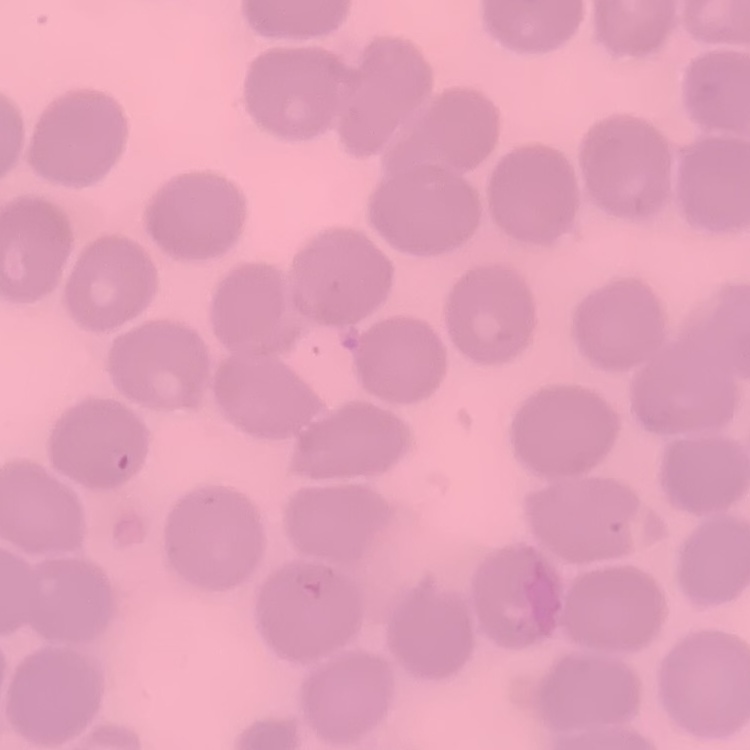
The red blood cells exhibit no rouleaux formation. Field's or Giemsa stain. One tile cut from a larger photomicrograph. Thin blood smear.